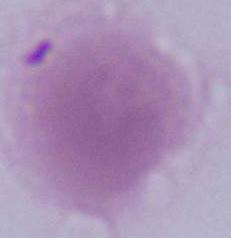

Summary:
  - Modality: photomicrograph
  - Identification: erythrocyte
  - Magnification: 1000x